Assess the morphology of the red blood cells.
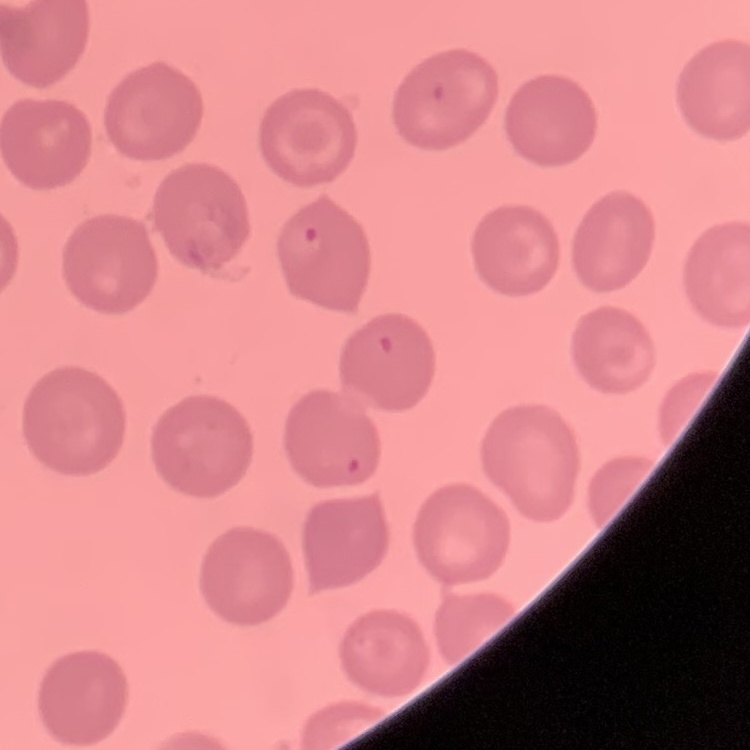

No rouleaux formation.

Summary:
  - Stain: Field's or Giemsa
  - Image type: square crop of a larger photomicrograph
  - Preparation: thin peripheral smear